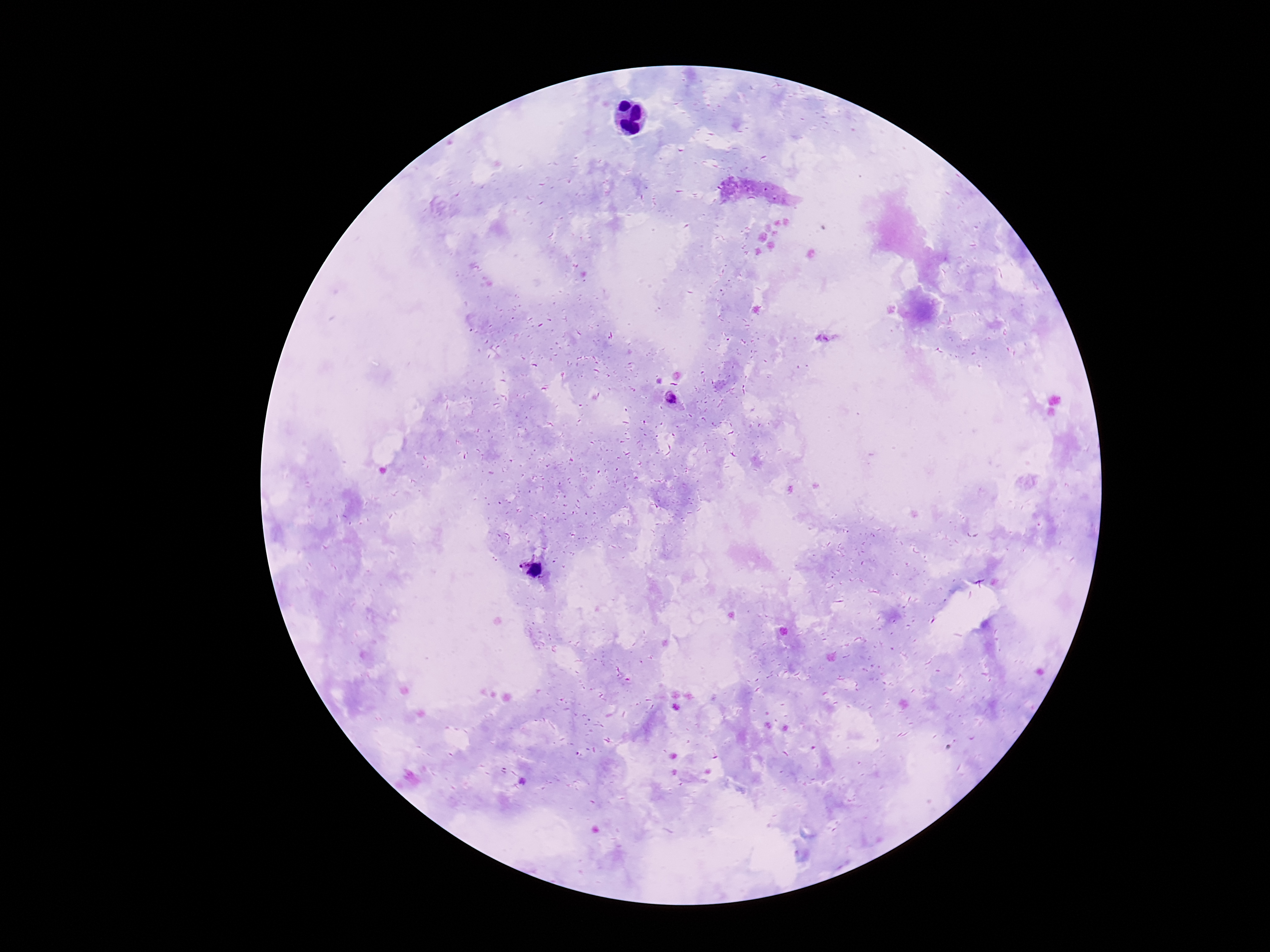

Approximate centers as [x, y] in pixels.
Summary:
  - Plasmodium parasite locations: [671, 399], [531, 567]
  - Field of view: single
  - Preparation: thick peripheral-blood smear
  - Image size: 1270×952 pixels
  - Patient malaria status: positive
  - Stain: Giemsa
  - Capture: smartphone camera through the microscope eyepiece
  - Magnification: 100x